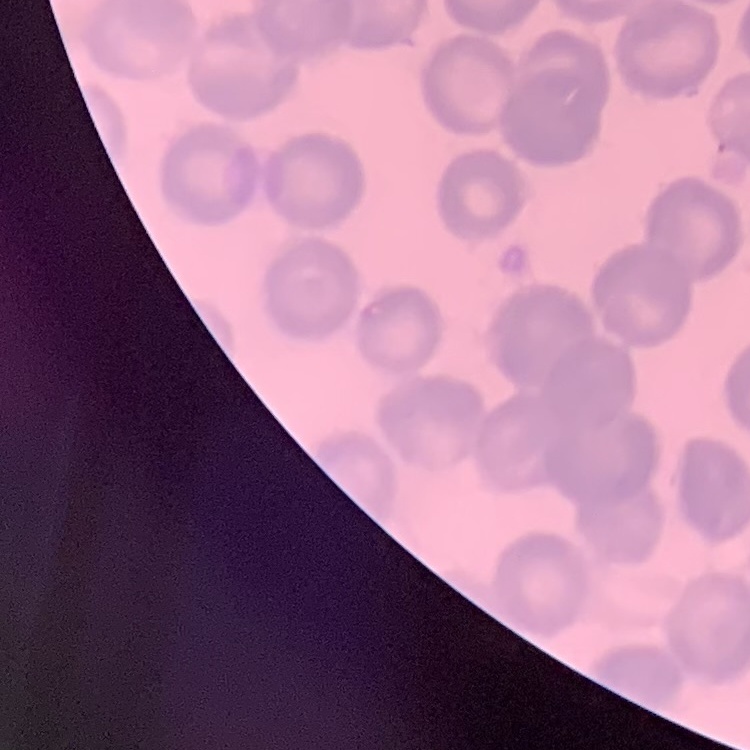

The erythrocytes show no rouleaux formation. Thin blood smear. One tile cut from a larger photomicrograph. Field's or Giemsa stain.